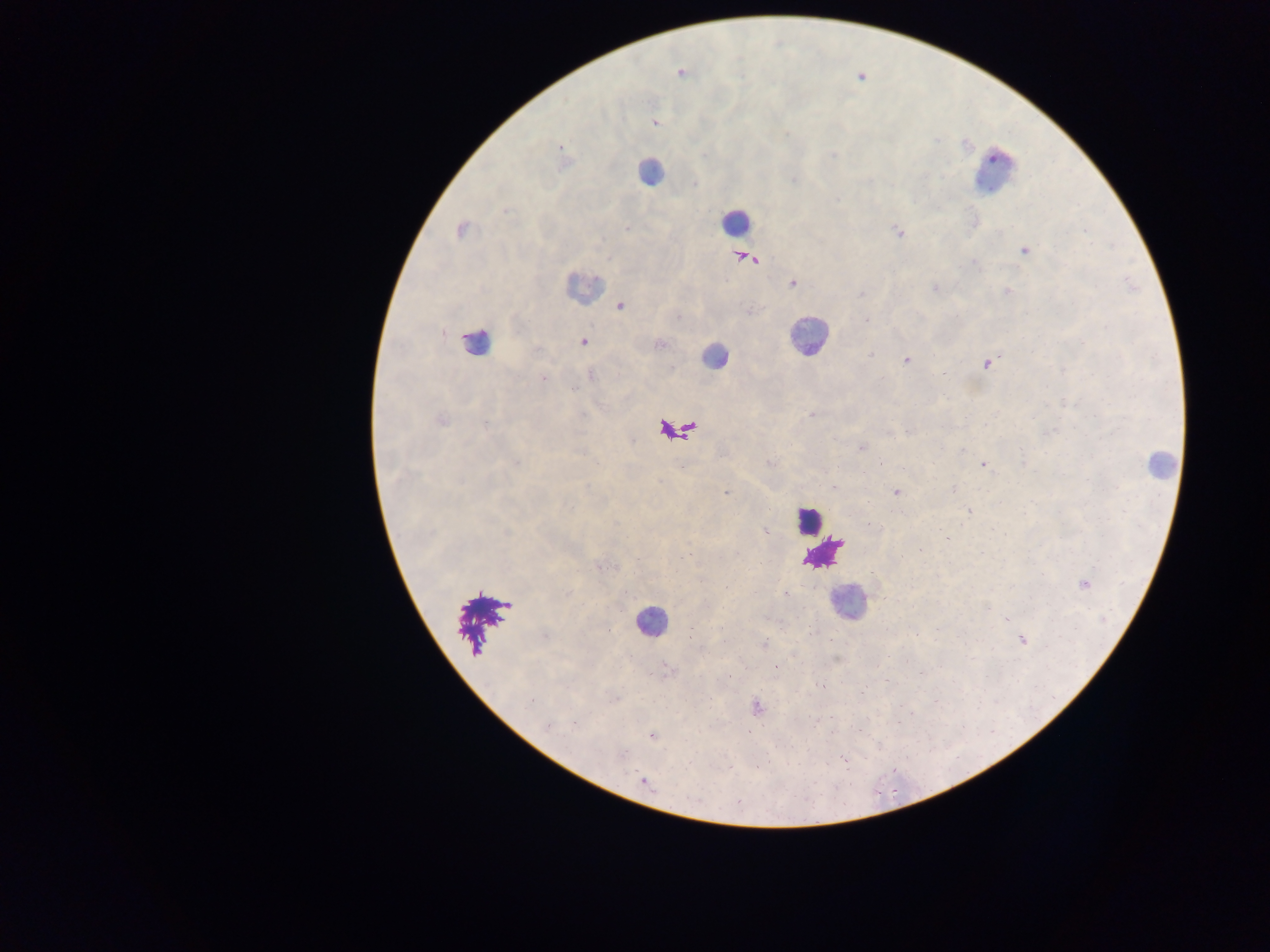

leukocyte locations = approximate centers as {x, y} in pixels: {649, 171}, {994, 171}, {734, 221}, {582, 288}, {806, 335}, {475, 343}, {713, 356}, {678, 429}, {1159, 465}, {807, 520}, {823, 551}, {848, 601}, {478, 621}, {650, 621}
country = Ghana
capture = mobile-phone photograph through a microscope
Plasmodium parasite locations = approximate centers as {x, y} in pixels: {681, 73}, {859, 76}, {653, 121}, {559, 147}, {626, 228}, {461, 229}, {900, 233}, {1024, 250}, {741, 257}, {750, 257}, {791, 282}, {935, 288}, {1007, 291}, {620, 305}, {867, 320}, {582, 342}, {658, 344}, {906, 360}, {986, 363}, {942, 375}, {542, 377}, {812, 414}, {440, 420}, {908, 430}, {861, 447}, {983, 464}, {833, 486}, {953, 489}, {895, 492}, {726, 493}, {969, 511}, {765, 531}, {945, 537}, {598, 566}, {1083, 583}, {1022, 639}, {776, 667}, {920, 672}, {861, 692}, {756, 708}, {574, 723}, {652, 736}, {643, 779}
image size = 1270×952 pixels
field of view = single
preparation = thick blood smear